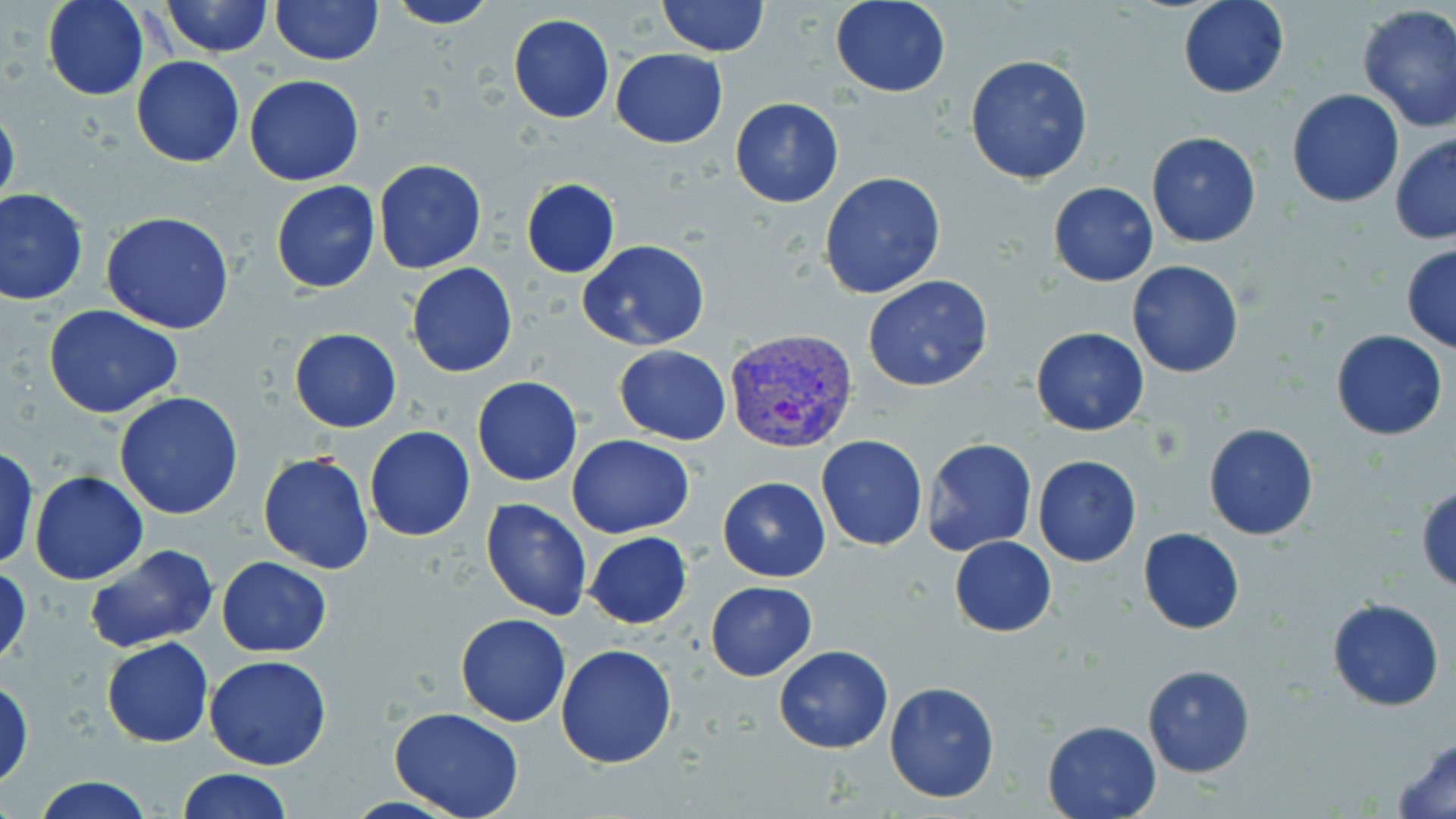
{
  "slide_level_diagnosis": "Plasmodium vivax",
  "stain": "May-Grünwald-Giemsa",
  "image_size": "1456×819 pixels",
  "field_of_view": "one of a larger specimen",
  "magnification": "1000x",
  "uninfected_red_blood_cell_locations": "approximate bounding boxes as (x1, y1, x2, y2) in pixels: (42, 0, 149, 101), (161, 0, 272, 58), (270, 0, 381, 65), (657, 0, 770, 56), (1177, 0, 1289, 99), (384, 1, 497, 29), (830, 1, 951, 96), (1355, 3, 1456, 132), (508, 12, 616, 123), (610, 49, 728, 148), (964, 55, 1094, 184), (131, 56, 245, 167), (245, 73, 364, 185), (1285, 89, 1405, 209), (729, 98, 844, 208), (0, 99, 20, 218), (1145, 130, 1261, 248), (1390, 131, 1456, 244), (373, 158, 486, 273), (819, 171, 946, 300), (520, 178, 621, 277), (271, 180, 380, 293), (1048, 181, 1158, 286), (1, 188, 89, 307), (102, 210, 235, 333), (578, 241, 711, 350), (1400, 245, 1456, 353), (1126, 259, 1244, 379), (406, 262, 518, 379), (862, 274, 994, 391), (44, 305, 186, 419), (1030, 326, 1149, 436), (290, 328, 401, 432), (1331, 330, 1448, 441), (614, 344, 731, 445), (473, 376, 583, 487), (113, 392, 244, 520), (1202, 422, 1319, 541), (365, 426, 475, 541), (568, 435, 694, 538), (816, 435, 926, 551), (921, 438, 1036, 557), (0, 447, 39, 571), (258, 449, 374, 575), (1032, 454, 1141, 567), (28, 471, 149, 586), (717, 476, 830, 582), (1416, 485, 1456, 592), (480, 498, 594, 621), (1137, 526, 1243, 635), (584, 531, 693, 629), (949, 536, 1057, 637), (84, 544, 220, 655), (217, 556, 332, 657), (1, 563, 32, 670), (705, 580, 818, 682), (1326, 598, 1444, 711), (456, 613, 571, 726), (102, 637, 213, 747), (555, 643, 678, 769), (772, 645, 893, 752), (204, 656, 331, 771), (1141, 664, 1255, 777), (0, 675, 34, 789), (884, 681, 1000, 804), (390, 708, 526, 819), (1041, 719, 1164, 818), (1392, 734, 1456, 819), (176, 768, 292, 819), (31, 775, 156, 818)",
  "plasmodium_vivax_infected_red_blood_cell_locations": "approximate bounding boxes as (x1, y1, x2, y2) in pixels: (726, 328, 859, 454)",
  "modality": "light microscopy",
  "preparation": "thin blood film"
}